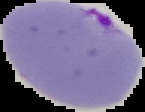

image type = segmented cell region with the area outside set to black
image size = 145×112 pixels
preparation = thin blood film
result = malaria parasites detected